Locate every Plasmodium ovale-infected red blood cell.
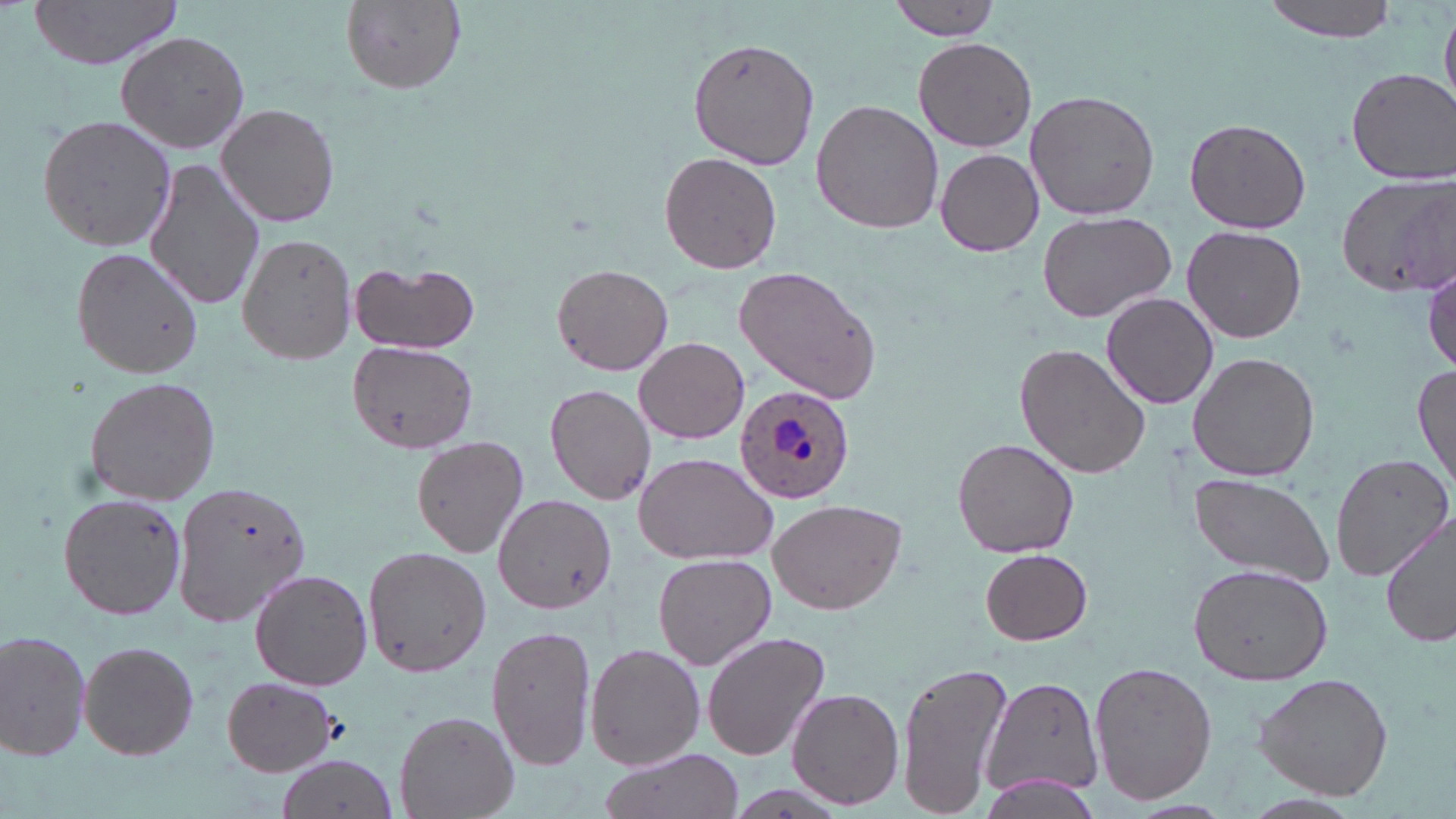

Approximate bounding boxes as (x1,y1)-(x2,y2) corner pairs in pixels.
Plasmodium ovale-infected red blood cells: (733,384)-(853,504).

Summary:
  - Uninfected red blood cell locations: (30,0)-(184,71), (338,0)-(468,95), (884,0)-(1000,40), (1262,0)-(1398,42), (1440,7)-(1455,108), (116,30)-(252,155), (687,31)-(820,170), (913,35)-(1036,154), (1343,68)-(1455,184), (1024,90)-(1161,221), (811,99)-(945,234), (217,102)-(341,228), (36,113)-(178,252), (1183,118)-(1311,234), (935,146)-(1045,259), (658,151)-(782,275), (145,160)-(267,313), (1335,174)-(1455,299), (1036,211)-(1176,322), (1181,227)-(1307,344), (238,232)-(360,364), (71,245)-(205,380), (350,262)-(479,355), (552,264)-(671,376), (733,267)-(882,403), (1100,291)-(1219,409), (635,336)-(750,444), (348,339)-(478,453), (1016,344)-(1150,479), (1187,351)-(1320,482), (1412,361)-(1455,491), (82,377)-(222,506), (544,384)-(656,504), (411,435)-(529,558), (952,436)-(1080,558), (1331,451)-(1453,579), (634,453)-(776,566), (1187,475)-(1336,583), (171,480)-(315,630), (58,493)-(187,619), (493,494)-(617,614), (766,496)-(910,615), (1380,514)-(1456,650), (363,544)-(488,678), (978,548)-(1094,645), (652,553)-(776,671), (1188,564)-(1331,683), (250,569)-(372,690), (487,624)-(596,772), (0,628)-(93,761), (701,632)-(831,762), (78,640)-(199,760), (587,644)-(703,769), (895,657)-(1014,819), (1089,660)-(1218,807), (1251,672)-(1394,799), (978,673)-(1105,802), (221,676)-(339,775), (788,689)-(903,809), (393,708)-(520,818), (596,747)-(744,819), (279,755)-(400,819)
  - Slide-level diagnosis: Plasmodium ovale
  - Modality: optical microscopy
  - Preparation: thin blood film
  - Magnification: 1000x
  - Stain: May-Grünwald-Giemsa
  - Field of view: single
  - Image size: 1456×819 pixels